Report the malaria status of this cell.
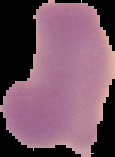

Uninfected.

Cell region segmented out of the field of view; the surrounding area is masked to black. Image is 115×157 pixels. From a thin blood film.